Report the malaria status of this cell.
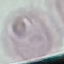

It is uninfected.

Summary:
  - Capture: smartphone camera at the microscope eyepiece
  - Image type: cell patch, automatically extracted from a larger field of view and resized to 64 × 64 pixels
  - Stain: Giemsa
  - Preparation: thin smear